Describe the morphology of the erythrocytes.
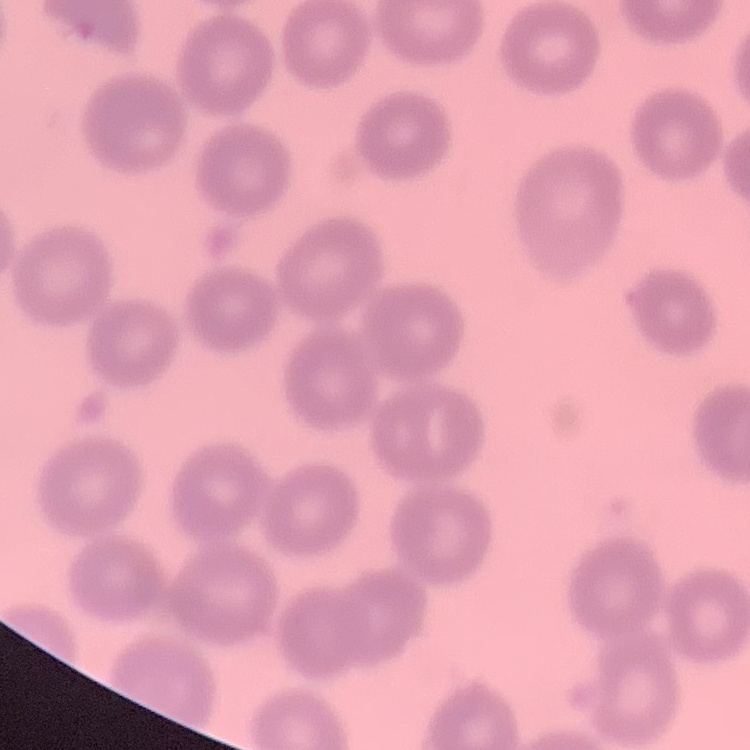
No rouleaux formation.

Summary:
  - Stain: Field's or Giemsa
  - Preparation: thin blood smear
  - Image type: one tile cut from a larger photomicrograph